Report the malaria status of this cell.
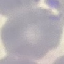

It is uninfected.

capture = smartphone camera at the microscope eyepiece
preparation = thin blood film
image type = automatically extracted cell patch, resized to 64 × 64 pixels
stain = Giemsa